Report the malaria status of this cell.
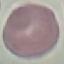
Uninfected.

Summary:
  - Image type: automatically extracted cell patch, resized to 64 × 64 pixels
  - Capture: smartphone camera at the microscope eyepiece
  - Stain: Giemsa
  - Preparation: thin smear